Assess the morphology of the erythrocytes.
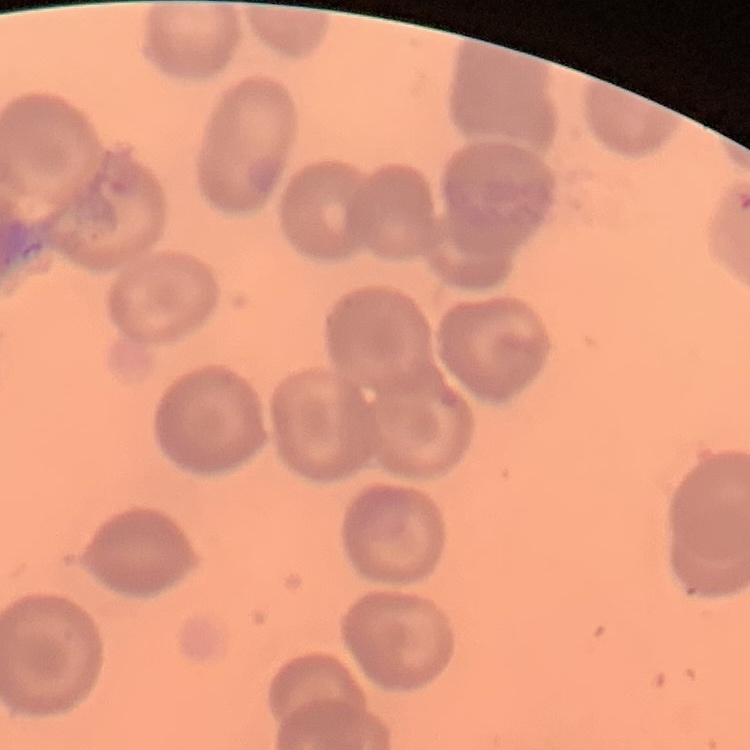

No rouleaux formation.

Field's or Giemsa stain. One tile cut from a larger photomicrograph. Thin peripheral smear.